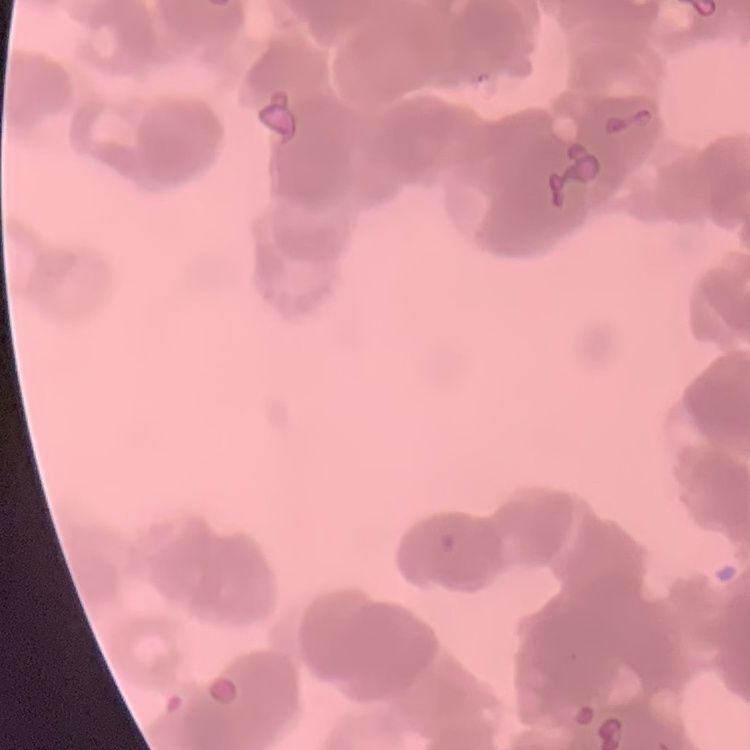

Summary:
  - Erythrocyte morphology: rouleaux formation
  - Image type: one tile cut from a larger photomicrograph
  - Stain: Field's or Giemsa
  - Preparation: thin peripheral smear